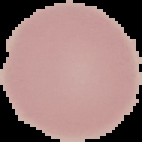
From a thin blood smear. The area outside the segmented cell region is set to black. Image is 142×142 pixels. Result: no Plasmodium parasites seen.